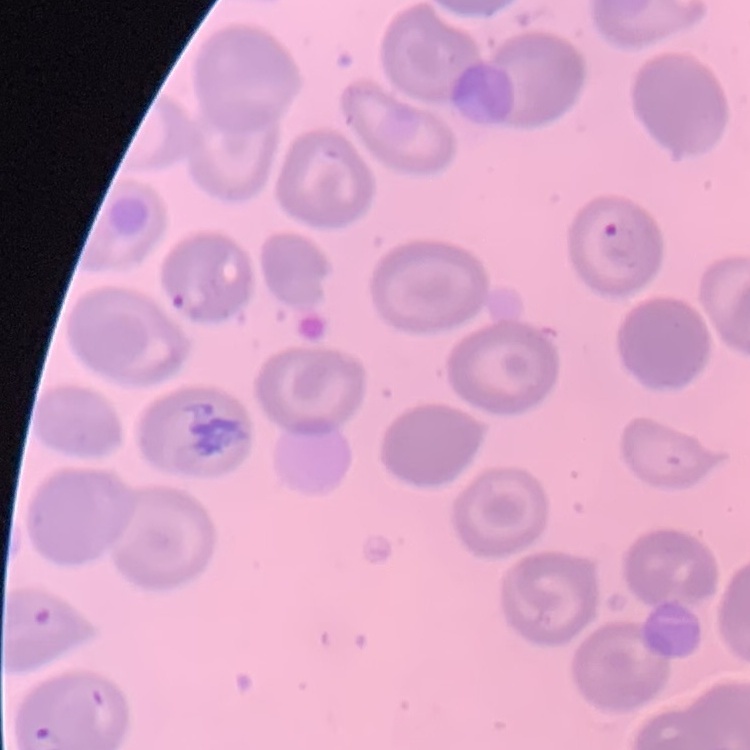
erythrocyte_morphology: no rouleaux formation
image_type: one tile cut from a larger photomicrograph
preparation: thin blood film
stain: Field's or Giemsa